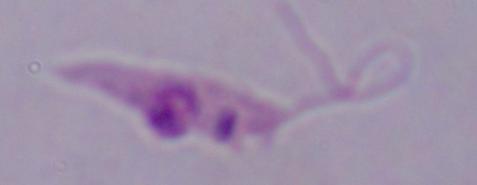
identification = Leishmania
magnification = 1000x
modality = photomicrograph